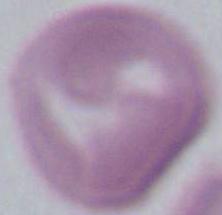

{
  "identification": "red blood cell",
  "modality": "photomicrograph",
  "magnification": "1000x"
}